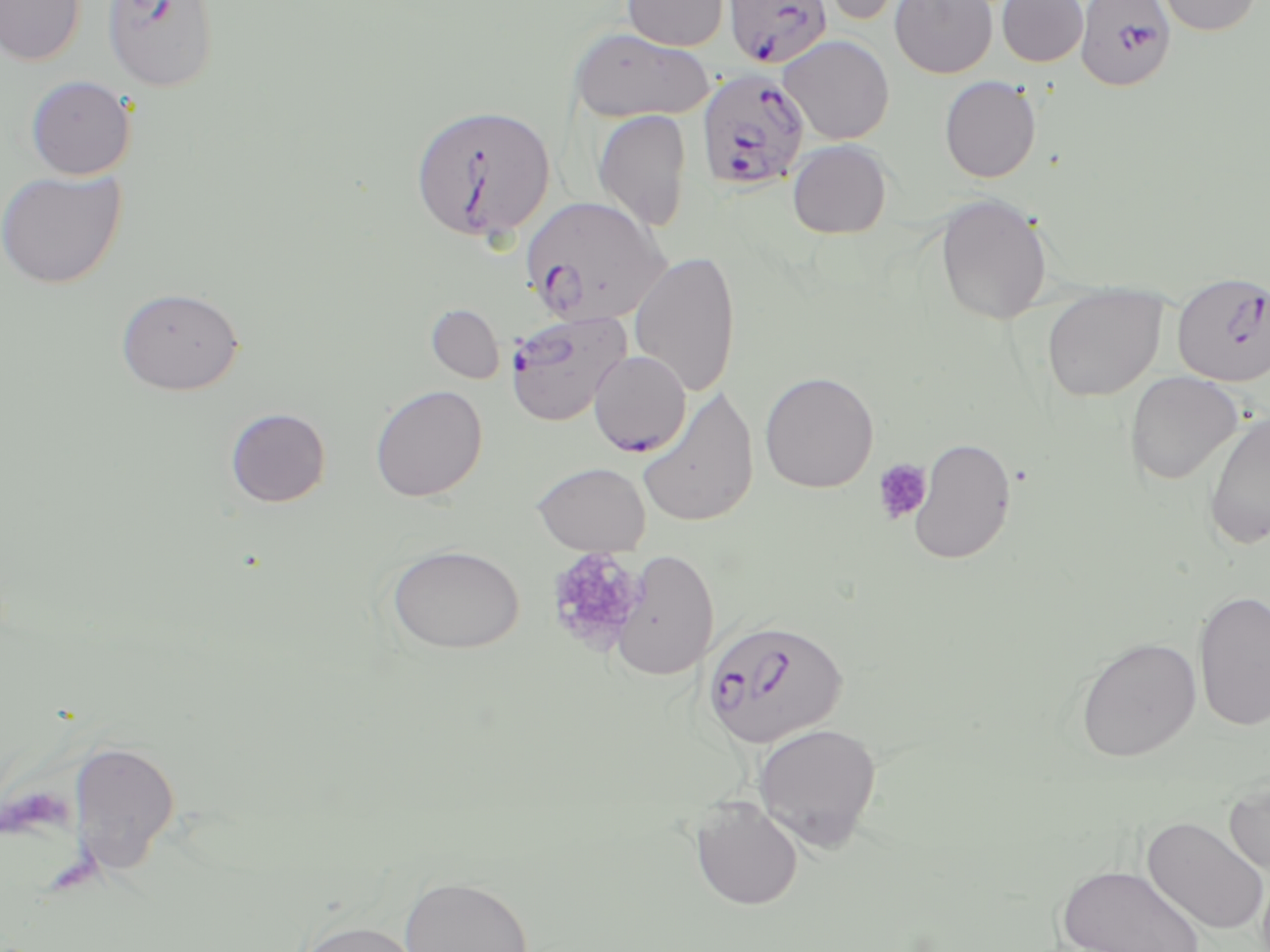

Approximate bounding boxes as [x1, y1, x2, y2] in pixels. Platelet locations: [872, 458, 934, 524], [544, 547, 647, 654]. Uninfected red blood cell locations: [1, 0, 86, 66], [622, 0, 728, 51], [810, 0, 918, 27], [890, 0, 998, 78], [997, 0, 1088, 67], [1155, 0, 1262, 36], [568, 27, 713, 123], [778, 34, 895, 144], [25, 75, 136, 180], [939, 76, 1041, 182], [592, 109, 692, 231], [787, 139, 892, 239], [0, 169, 127, 289], [935, 193, 1053, 325], [629, 249, 740, 398], [1041, 283, 1167, 402], [116, 286, 244, 395], [427, 304, 504, 383], [759, 370, 879, 493], [1124, 371, 1244, 485], [370, 384, 488, 502], [636, 385, 759, 528], [225, 407, 331, 507], [1203, 410, 1270, 550], [908, 436, 1017, 565], [531, 461, 651, 554], [385, 543, 525, 655], [610, 549, 720, 681], [1193, 590, 1270, 732], [1075, 636, 1201, 762], [752, 722, 882, 851], [68, 738, 181, 877], [1224, 775, 1270, 878], [690, 796, 803, 910], [1142, 816, 1269, 935], [1056, 863, 1205, 952], [399, 875, 533, 951], [294, 918, 424, 952]. Plasmodium falciparum-infected red blood cell locations: [102, 0, 219, 92], [728, 0, 832, 71], [1075, 0, 1176, 91], [695, 67, 810, 192], [409, 103, 556, 244], [520, 195, 672, 326], [1171, 270, 1270, 385], [504, 310, 632, 426], [588, 349, 691, 457], [701, 618, 850, 751]. Slide-level diagnosis: Plasmodium falciparum. Thin blood film. Image is 1270×952 pixels. Captured at 1000x magnification. Light microscopy. May-Grünwald-Giemsa stain. One field of a larger specimen.